Outline each blood parasite and name the species.
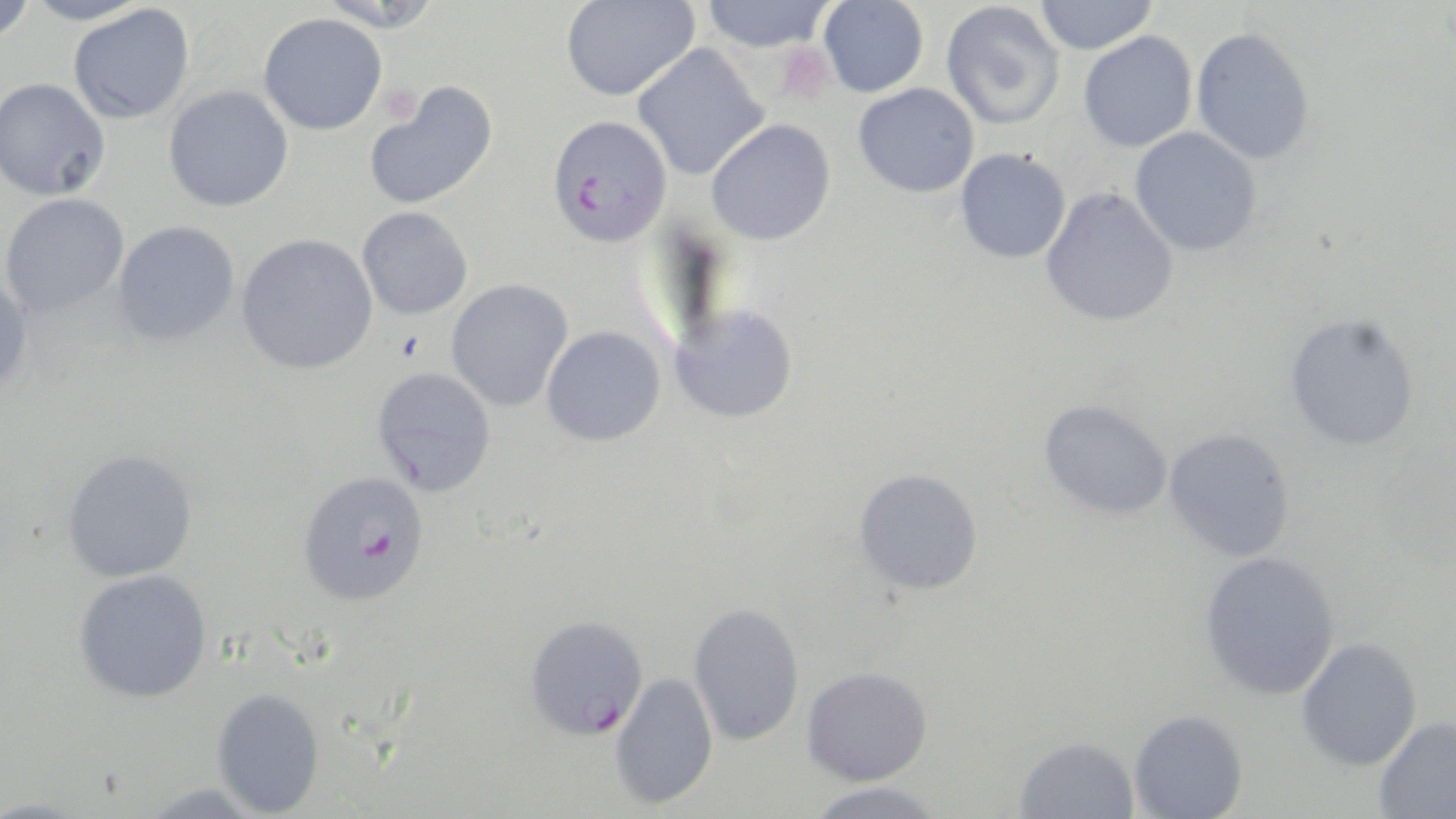

Approximate bounding boxes as [x1, y1, x2, y2] in pixels.
Plasmodium falciparum-infected red blood cells: [546, 115, 672, 247], [297, 471, 430, 606], [524, 614, 649, 740].
No Plasmodium ovale, Plasmodium malariae, Plasmodium vivax, Babesia divergens, or Trypanosoma brucei observed.

Platelet locations: [776, 44, 836, 104], [378, 83, 421, 126]. Uninfected red blood cell locations: [0, 0, 37, 45], [22, 0, 154, 26], [315, 0, 446, 32], [698, 0, 836, 52], [1034, 0, 1158, 55], [560, 1, 698, 102], [818, 1, 929, 98], [941, 2, 1065, 130], [68, 4, 195, 124], [258, 13, 387, 135], [1190, 27, 1314, 165], [1078, 31, 1197, 153], [631, 43, 768, 181], [0, 78, 111, 201], [364, 81, 499, 211], [853, 83, 979, 198], [164, 85, 294, 212], [706, 119, 836, 246], [1129, 128, 1262, 257], [955, 148, 1071, 264], [1040, 187, 1179, 328], [0, 193, 129, 318], [357, 207, 473, 320], [112, 221, 240, 347], [236, 233, 378, 375], [0, 274, 34, 399], [445, 279, 574, 412], [669, 305, 798, 424], [1283, 313, 1421, 452], [541, 326, 666, 447], [371, 367, 497, 497], [1038, 399, 1174, 521], [1163, 427, 1297, 562], [62, 449, 198, 583], [852, 468, 984, 596], [1199, 551, 1340, 701], [74, 569, 212, 703], [688, 602, 805, 745], [1296, 638, 1423, 771], [801, 666, 933, 785], [609, 673, 718, 810], [211, 687, 325, 816], [1128, 709, 1248, 819], [1374, 716, 1456, 818], [1014, 736, 1139, 819], [804, 782, 949, 819], [137, 783, 268, 818]. Slide-level diagnosis: Plasmodium falciparum. Captured at 1000x magnification. Image is 1456×819 pixels. Thin blood film. May-Grünwald-Giemsa-stained preparation. One field of a larger specimen. Light microscopy.